Assess this cell for malaria.
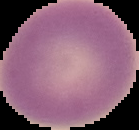

It is uninfected.

From a thin blood smear. Image is 139×130 pixels. The area outside the segmented cell region is set to black.